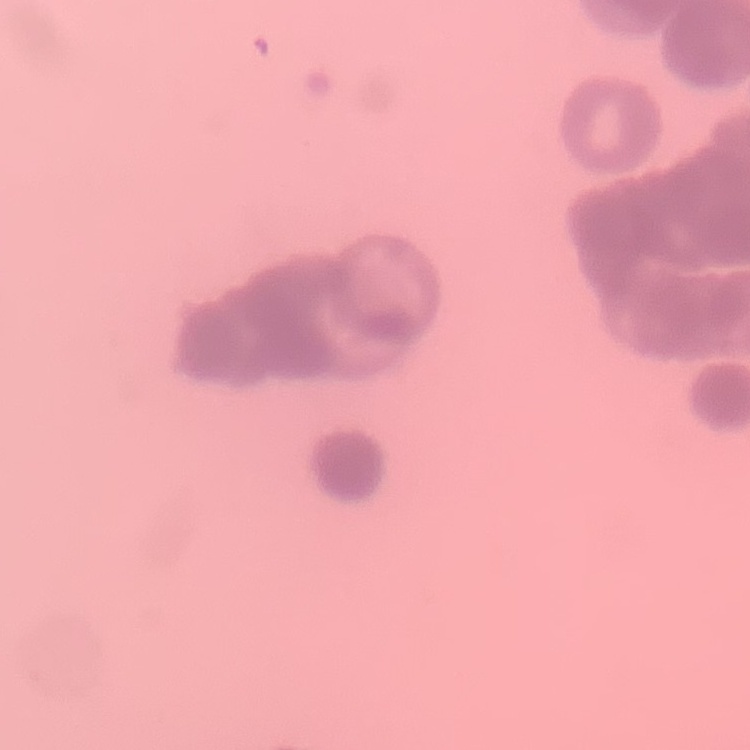

The red blood cells exhibit rouleaux formation. Square crop of a larger photomicrograph. Stained with either Field's or Giemsa. Thin blood smear.